Describe the morphology of the erythrocytes.
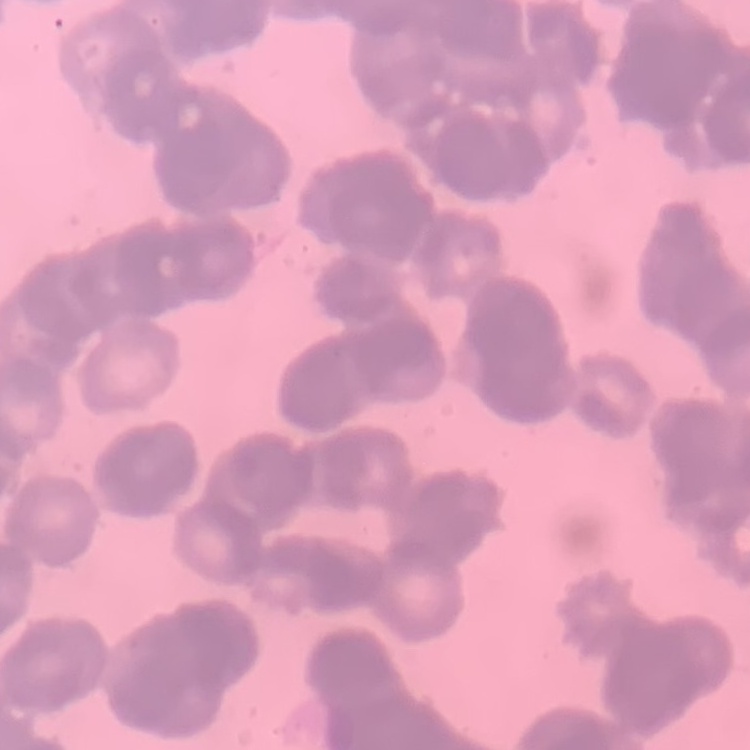
They show rouleaux formation.

Summary:
  - Stain: Field's or Giemsa
  - Image type: one tile cut from a larger photomicrograph
  - Preparation: thin blood smear